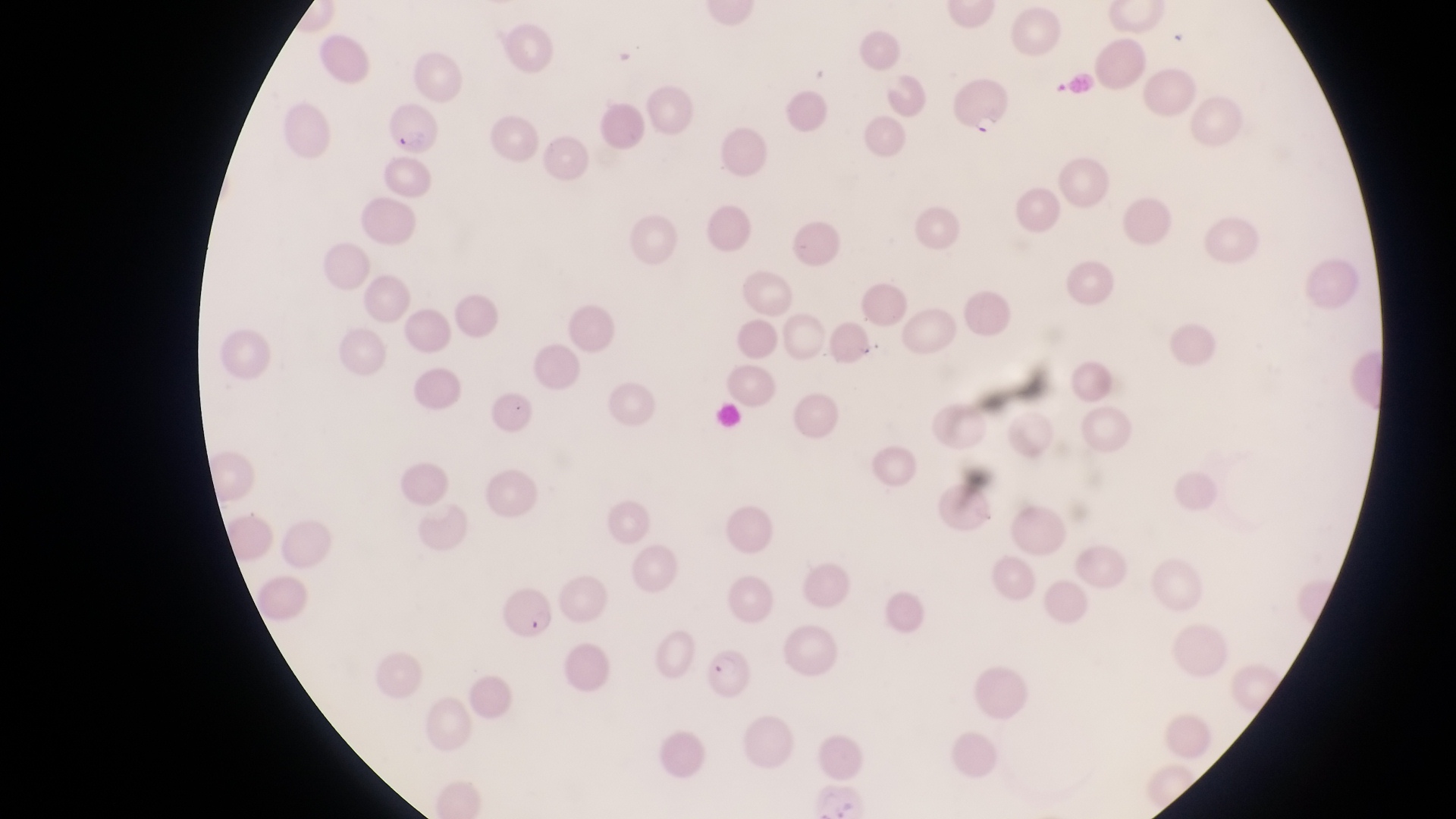
capture = smartphone photograph through the eyepiece of an Olympus CX-23 microscope
image size = 1456×819 pixels
field of view = single
country = Uganda
trophozoite locations = approximate bounding boxes as [left, top, right, bottom] in pixels: [977, 109, 1001, 139]
magnification = 1000x
parasitised red blood cell locations = approximate bounding boxes as [left, top, right, bottom] in pixels: [384, 106, 437, 159], [497, 587, 553, 639], [704, 645, 760, 703]
preparation = thin blood film